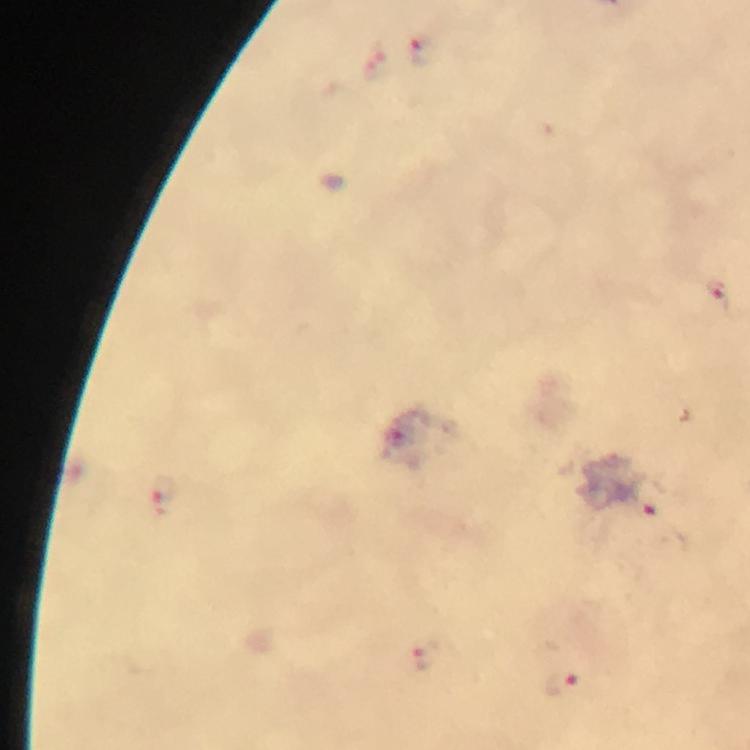
Approximate centers as {x, y} in pixels. Malaria parasite locations: {421, 50}, {376, 62}, {717, 288}, {162, 493}, {648, 497}, {425, 657}, {560, 681}. A crop from one field of view. Immersion oil applied. Photographed with a smartphone mounted on the microscope. Thick smear. 100x magnification. From a malaria diagnostic workup. Giemsa-stained preparation. Image is 750×750 pixels.